Classify this cell by malaria status.
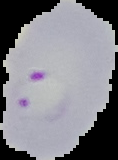

It is parasitized.

Segmented cell region on a black background. From a thin blood film. Image is 118×160 pixels.